Assess this cell for malaria.
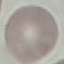
Uninfected.

Thin blood smear. Automatically extracted cell patch, resized to 64 × 64 pixels. Acquired by smartphone through the microscope eyepiece. Giemsa stain.